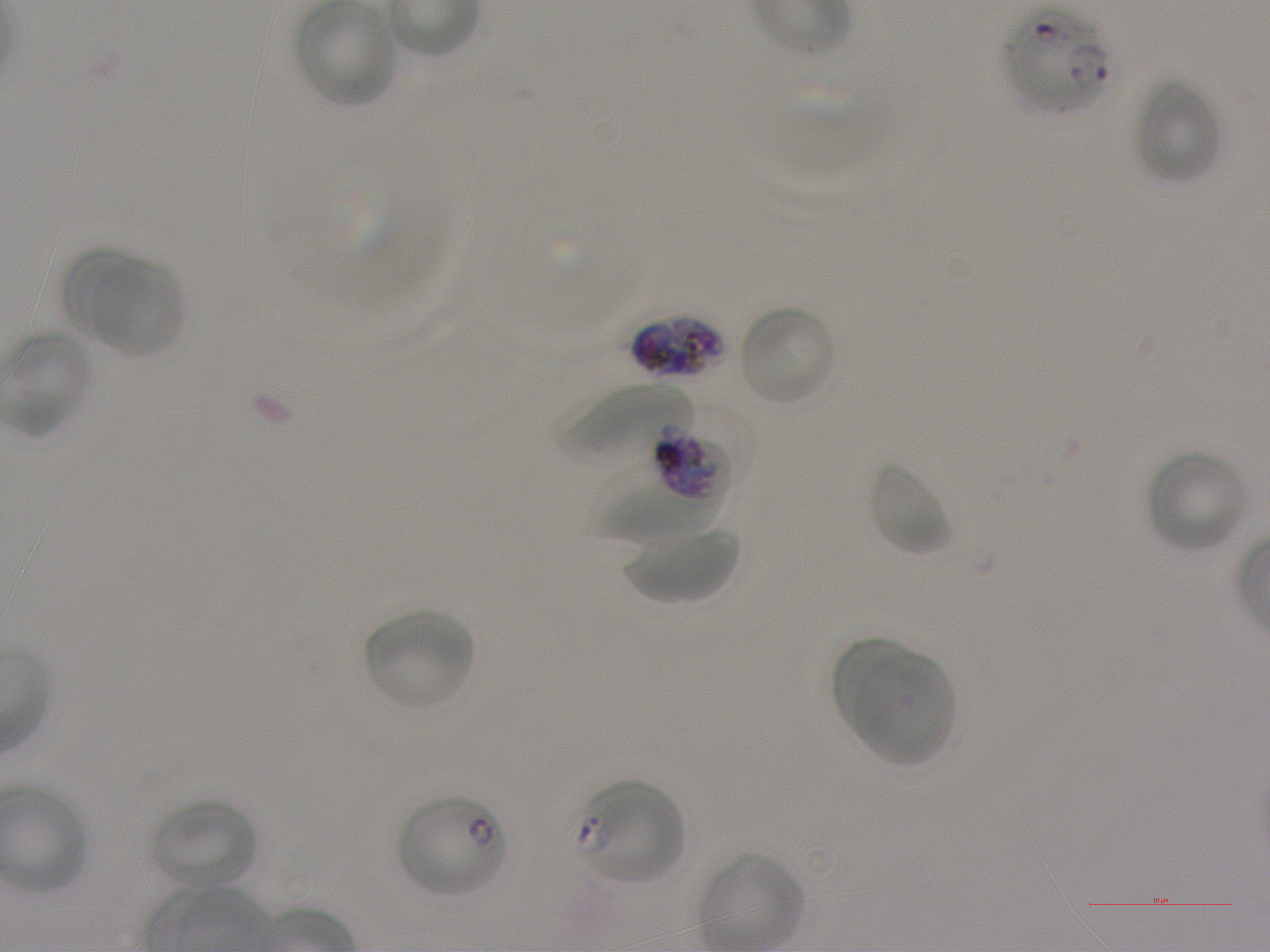
Not every red blood cell is marked. A life-cycle stage — or a range of stages, where the recorded stages span more than one — follows each staged infected red blood cell.
locations of infected red blood cells = approximate bounding boxes as (x1, y1, x2, y2) in pixels: (1007, 10, 1113, 114); (632, 314, 733, 383); (650, 427, 731, 503) late trophozoite to late schizont; (578, 780, 684, 885) early ring to early trophozoite; (395, 795, 506, 898) ring
donor blood group = A+
locations of red blood cells of indeterminate infection status = approximate bounding boxes as (x1, y1, x2, y2) in pixels: (592, 459, 724, 545)
culture = in-vitro P. falciparum strain NF54, static
objective = 100x, oil immersion, numerical aperture 1.25
image size = 1270×952 pixels
preparation = thin blood film
stain = Giemsa
field of view = one from this slide
locations of uninfected red blood cells = approximate bounding boxes as (x1, y1, x2, y2) in pixels: (296, 1, 397, 107), (1135, 80, 1223, 185), (67, 251, 155, 348), (90, 259, 185, 358), (737, 304, 838, 406), (558, 384, 693, 465), (1146, 450, 1247, 552), (868, 461, 952, 557), (625, 525, 741, 605), (364, 610, 475, 711), (831, 636, 916, 733), (851, 647, 956, 768), (150, 798, 258, 890)